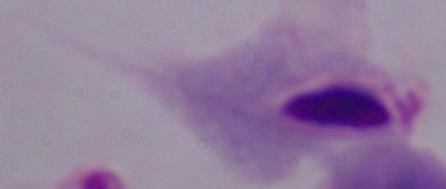

Summary:
  - Magnification: 1000x
  - Modality: photomicrograph
  - Identification: trichomonad